Name the parasite shown.
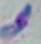
Toxoplasma gondii.

magnification: 1000x
modality: photomicrograph